Locate every Plasmodium parasite.
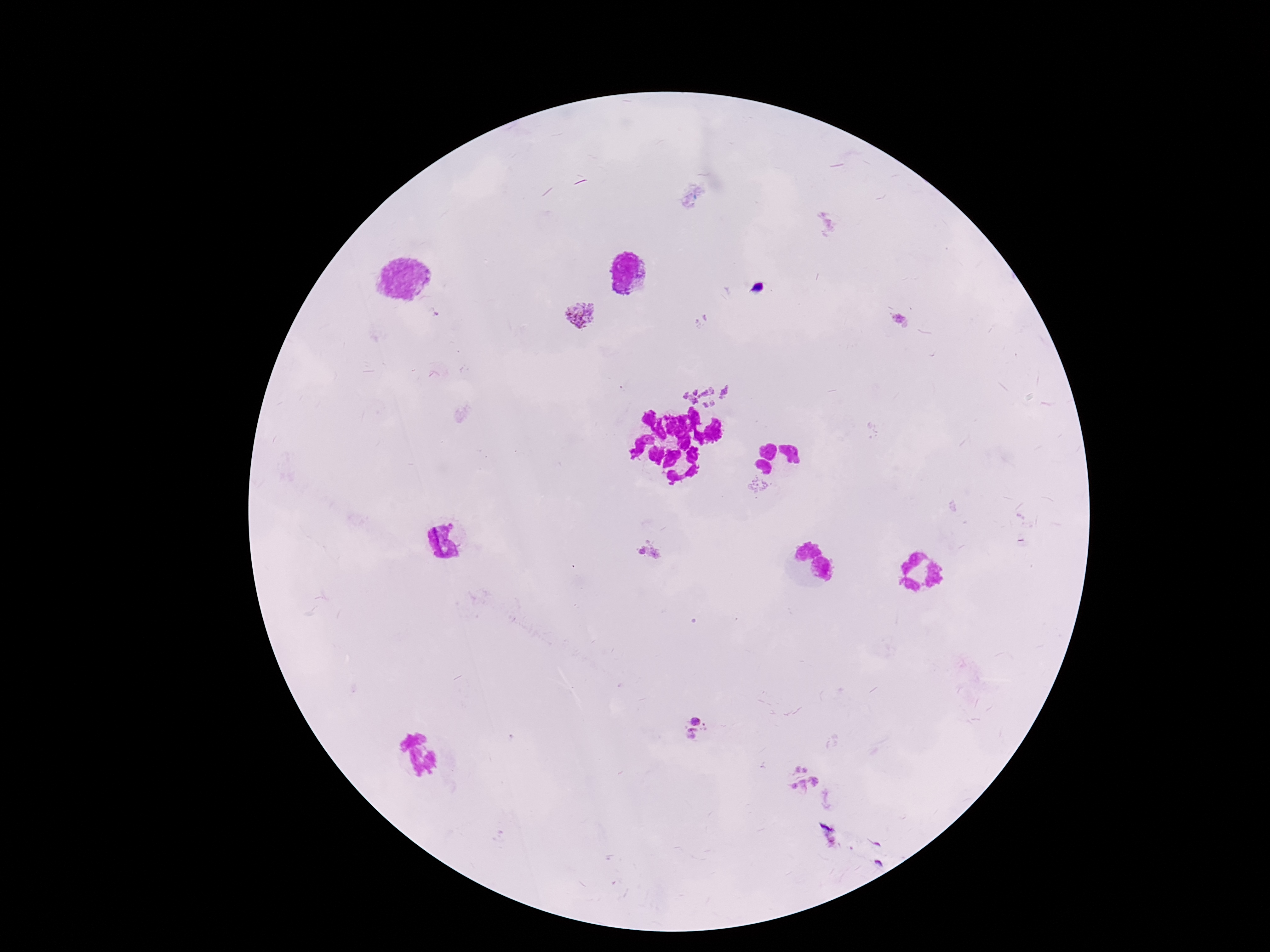

Approximate centers as (x, y) in pixels.
Plasmodium parasites: (580, 313), (899, 321), (710, 382), (757, 487), (648, 550), (698, 717), (695, 738), (801, 766), (815, 781), (794, 786), (803, 786).

Thick blood film. Photographed through the microscope eyepiece with a smartphone camera. Single field of view. 100x magnification. Giemsa stain. Patient malaria status: infected. Image is 1270×952 pixels.